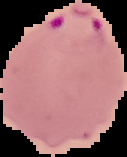
Summary:
  - Image type: segmented cell region with the area outside set to black
  - Image size: 127×157 pixels
  - Result: malaria parasites detected
  - Preparation: thin blood smear